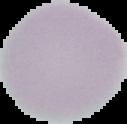 Image is 127×124 pixels. Segmented cell region on a black background. From a thin blood film. Result: no Plasmodium parasites seen.